Locate every Plasmodium malariae-infected red blood cell.
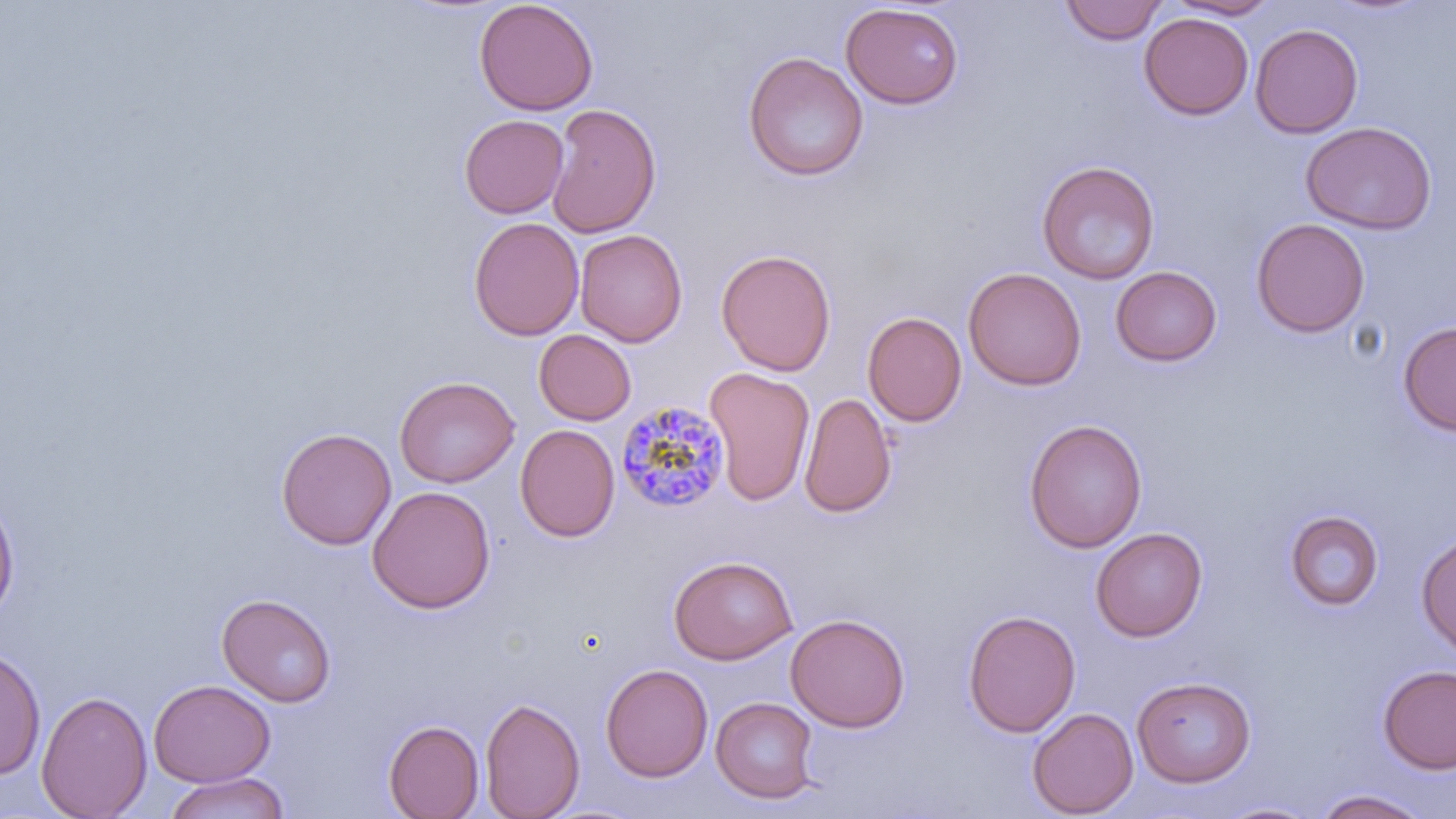

Approximate bounding boxes as [x1, y1, x2, y2] in pixels.
Plasmodium malariae-infected red blood cells: [616, 399, 732, 513].

{
  "slide_level_diagnosis": "Plasmodium malariae",
  "uninfected_red_blood_cell_locations": "approximate bounding boxes as [x1, y1, x2, y2] in pixels: [474, 0, 599, 116], [1060, 0, 1167, 45], [1164, 0, 1281, 20], [840, 3, 965, 110], [1139, 12, 1254, 120], [1250, 23, 1363, 138], [742, 51, 869, 181], [546, 103, 662, 238], [459, 114, 569, 219], [1300, 121, 1437, 234], [1036, 159, 1160, 284], [468, 216, 584, 341], [1251, 218, 1370, 338], [575, 229, 687, 347], [716, 248, 836, 376], [1110, 265, 1222, 366], [963, 267, 1086, 391], [862, 311, 967, 427], [1397, 321, 1456, 436], [534, 330, 636, 425], [704, 366, 815, 506], [394, 375, 519, 487], [799, 392, 897, 519], [1024, 418, 1147, 553], [515, 424, 620, 542], [276, 427, 396, 550], [367, 485, 496, 613], [0, 491, 20, 624], [1284, 509, 1384, 611], [1090, 526, 1208, 642], [1415, 532, 1456, 657], [668, 554, 798, 664], [217, 592, 336, 707], [962, 609, 1081, 738], [786, 613, 910, 733], [0, 645, 46, 781], [600, 662, 713, 782], [1377, 664, 1456, 774], [1131, 675, 1256, 787], [148, 679, 275, 787], [36, 689, 152, 819], [710, 696, 820, 803], [480, 697, 584, 818], [1027, 707, 1138, 818], [383, 719, 484, 818], [161, 772, 290, 819], [1313, 788, 1432, 818], [1214, 801, 1325, 819]",
  "magnification": "1000x",
  "modality": "light microscopy",
  "stain": "May-Grünwald-Giemsa",
  "field_of_view": "one of a larger specimen",
  "image_size": "1456×819 pixels",
  "preparation": "thin blood smear"
}